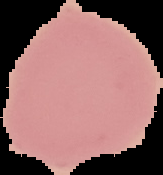
Summary:
  - Preparation: thin blood smear
  - Image size: 163×175 pixels
  - Image type: segmented cell region on a black background
  - Malaria status: uninfected